Point out each Plasmodium parasite.
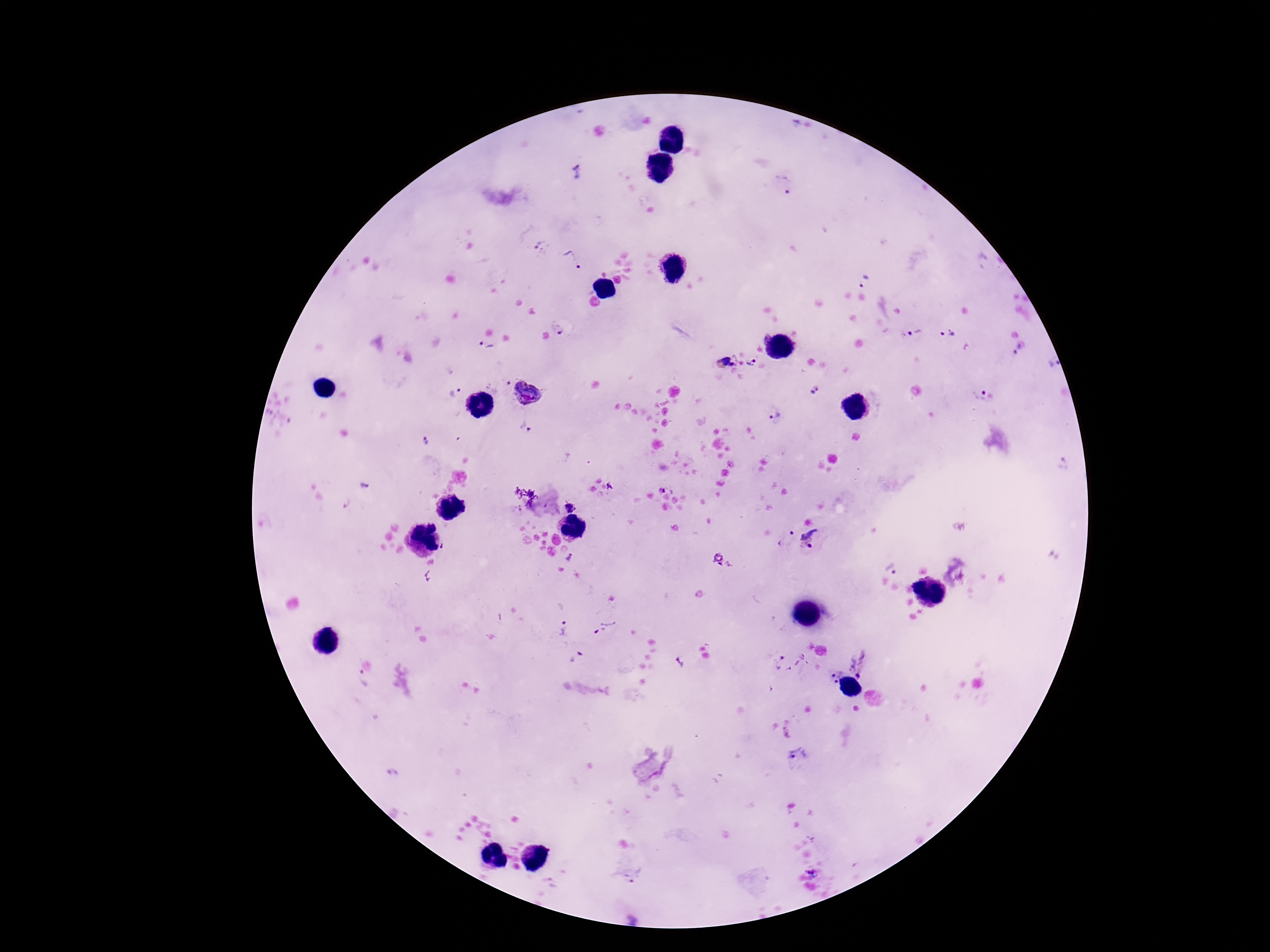

Approximate centers as (x, y) in pixels.
Plasmodium parasites: (577, 173), (782, 184), (539, 246), (573, 259), (863, 282), (560, 328), (947, 333), (915, 335), (485, 348), (1021, 348), (726, 362), (752, 363), (1053, 365), (506, 382), (815, 388), (452, 392), (529, 392), (978, 393), (774, 414), (526, 426), (426, 440), (610, 485), (362, 486), (662, 490), (569, 508), (792, 533), (808, 533), (443, 545), (810, 546), (718, 557), (570, 558), (720, 564), (729, 564), (890, 568), (606, 627), (563, 628), (781, 657), (576, 658), (679, 662), (833, 675), (859, 675), (835, 681), (796, 754), (812, 872), (635, 877).

Summary:
  - Field of view: single
  - Image size: 1270×952 pixels
  - Patient malaria status: positive
  - Stain: Giemsa
  - Magnification: 100x
  - Preparation: thick blood smear
  - Capture: smartphone camera through the microscope eyepiece